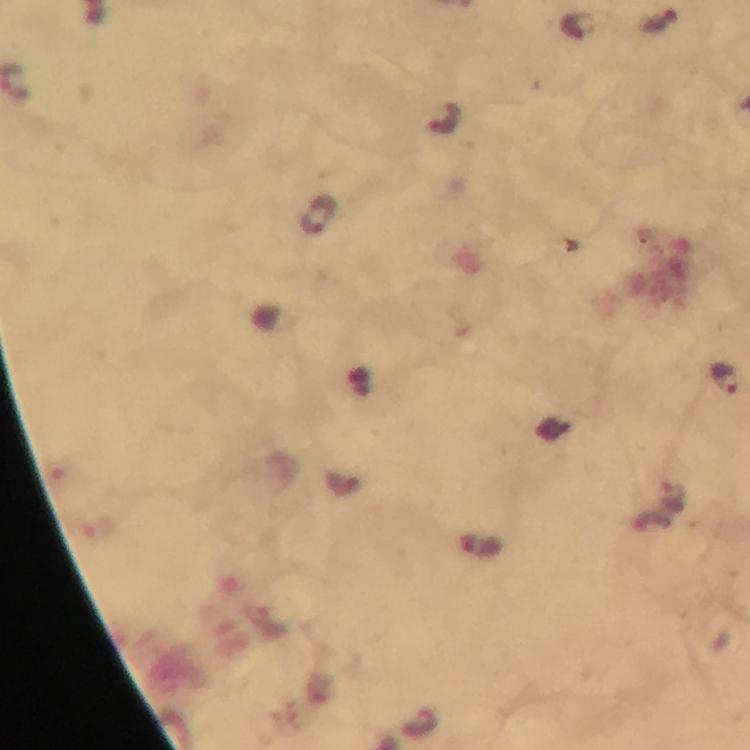
Approximate object centers, in pixels from the top-left corner. Plasmodium parasite locations: (x=660, y=20), (x=574, y=26), (x=446, y=118), (x=318, y=215), (x=725, y=379). Image is 750×750 pixels. From a diagnostic examination for malaria. Smartphone photograph taken through a microscope. Giemsa-stained preparation. Cropped region of a single field of view. Thick blood film. Immersion oil applied. At 100x magnification.